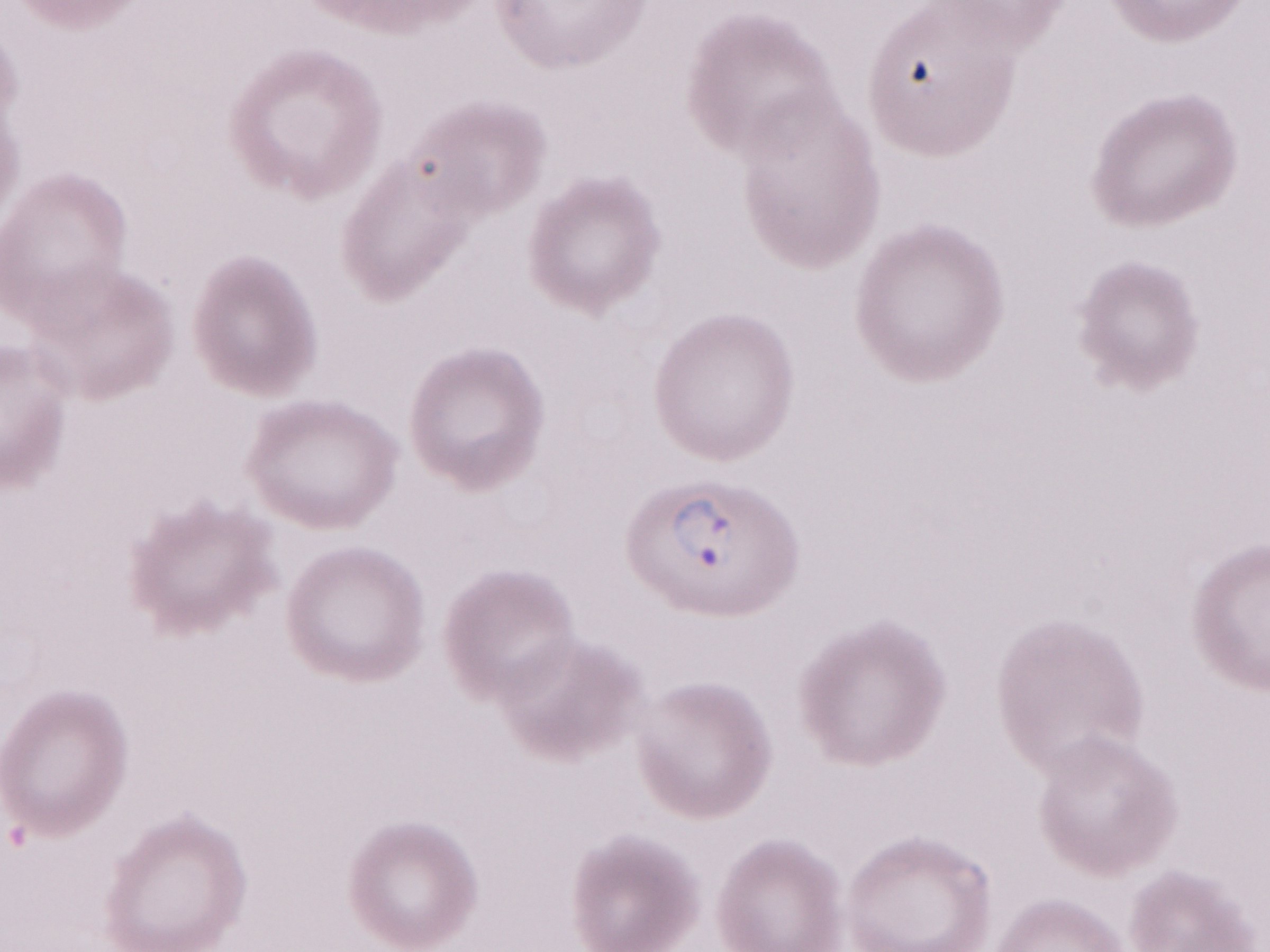 Single field of view. Thin peripheral-blood smear. Image is 1270×952 pixels. Magnification: 1,000x. Olympus BX43 microscope, Olympus DP73 camera. May-Grünwald-Giemsa stain. Patient diagnosis: malaria infection.